Outline each uninfected red blood cell.
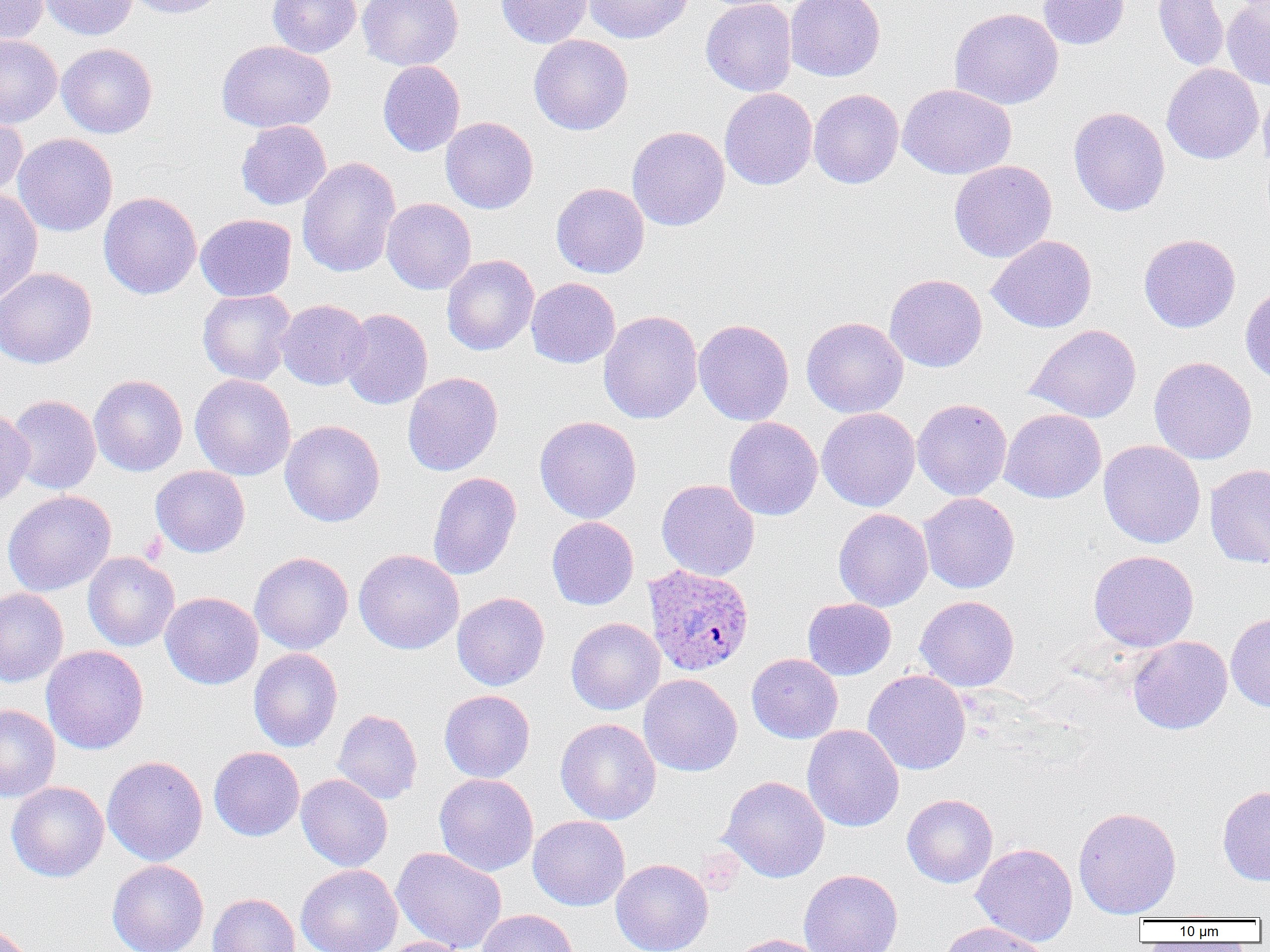
Approximate bounding boxes as named x1/y1/x2/y2 corners in pixels.
Uninfected red blood cells: (x1=0, y1=0, x2=48, y2=44), (x1=39, y1=0, x2=137, y2=40), (x1=124, y1=0, x2=228, y2=19), (x1=268, y1=0, x2=361, y2=58), (x1=358, y1=0, x2=463, y2=71), (x1=495, y1=0, x2=594, y2=48), (x1=584, y1=0, x2=692, y2=44), (x1=701, y1=0, x2=797, y2=96), (x1=785, y1=0, x2=885, y2=82), (x1=1037, y1=0, x2=1130, y2=49), (x1=1153, y1=0, x2=1229, y2=71), (x1=1222, y1=0, x2=1270, y2=90), (x1=949, y1=7, x2=1063, y2=110), (x1=529, y1=34, x2=633, y2=135), (x1=0, y1=35, x2=62, y2=128), (x1=216, y1=40, x2=336, y2=133), (x1=57, y1=43, x2=158, y2=138), (x1=378, y1=61, x2=465, y2=156), (x1=1162, y1=63, x2=1263, y2=164), (x1=897, y1=83, x2=1016, y2=179), (x1=1258, y1=83, x2=1270, y2=175), (x1=719, y1=88, x2=818, y2=190), (x1=809, y1=89, x2=904, y2=188), (x1=1068, y1=106, x2=1170, y2=217), (x1=0, y1=110, x2=27, y2=202), (x1=440, y1=116, x2=538, y2=213), (x1=236, y1=120, x2=331, y2=210), (x1=626, y1=125, x2=730, y2=231), (x1=13, y1=133, x2=117, y2=236), (x1=297, y1=157, x2=400, y2=277), (x1=949, y1=160, x2=1056, y2=262), (x1=551, y1=182, x2=650, y2=278), (x1=0, y1=189, x2=43, y2=304), (x1=99, y1=192, x2=201, y2=299), (x1=382, y1=198, x2=476, y2=294), (x1=196, y1=213, x2=296, y2=302), (x1=1138, y1=233, x2=1240, y2=333), (x1=987, y1=235, x2=1097, y2=333), (x1=442, y1=255, x2=538, y2=355), (x1=0, y1=267, x2=98, y2=368), (x1=884, y1=273, x2=987, y2=372), (x1=526, y1=277, x2=620, y2=368), (x1=1240, y1=284, x2=1270, y2=386), (x1=197, y1=289, x2=296, y2=385), (x1=276, y1=299, x2=370, y2=390), (x1=339, y1=308, x2=433, y2=410), (x1=598, y1=310, x2=703, y2=424), (x1=801, y1=317, x2=908, y2=418), (x1=693, y1=319, x2=794, y2=425), (x1=1025, y1=324, x2=1142, y2=423), (x1=1149, y1=356, x2=1257, y2=465), (x1=402, y1=372, x2=503, y2=476), (x1=89, y1=374, x2=188, y2=476), (x1=190, y1=374, x2=296, y2=481), (x1=6, y1=395, x2=101, y2=494), (x1=912, y1=398, x2=1012, y2=501), (x1=0, y1=406, x2=34, y2=509), (x1=817, y1=407, x2=920, y2=511), (x1=999, y1=409, x2=1106, y2=503), (x1=535, y1=415, x2=642, y2=523), (x1=723, y1=417, x2=823, y2=520), (x1=280, y1=420, x2=385, y2=527), (x1=1098, y1=440, x2=1205, y2=548), (x1=1205, y1=464, x2=1270, y2=568), (x1=150, y1=466, x2=250, y2=557), (x1=428, y1=472, x2=521, y2=580), (x1=656, y1=479, x2=760, y2=581), (x1=3, y1=490, x2=116, y2=596), (x1=918, y1=492, x2=1020, y2=594), (x1=833, y1=508, x2=933, y2=612), (x1=547, y1=517, x2=639, y2=610), (x1=354, y1=549, x2=464, y2=654), (x1=1088, y1=550, x2=1199, y2=652), (x1=249, y1=551, x2=354, y2=654), (x1=83, y1=552, x2=180, y2=651), (x1=0, y1=588, x2=68, y2=687), (x1=160, y1=592, x2=263, y2=689), (x1=452, y1=592, x2=550, y2=690), (x1=915, y1=595, x2=1019, y2=692), (x1=803, y1=598, x2=896, y2=680), (x1=1226, y1=612, x2=1270, y2=712), (x1=566, y1=617, x2=665, y2=715), (x1=1128, y1=636, x2=1232, y2=734), (x1=41, y1=645, x2=148, y2=754), (x1=248, y1=648, x2=343, y2=752), (x1=746, y1=653, x2=843, y2=743), (x1=863, y1=670, x2=971, y2=775), (x1=639, y1=673, x2=742, y2=776), (x1=439, y1=690, x2=535, y2=783), (x1=0, y1=705, x2=61, y2=802), (x1=332, y1=709, x2=423, y2=805), (x1=555, y1=718, x2=661, y2=824), (x1=802, y1=724, x2=904, y2=832), (x1=209, y1=746, x2=304, y2=841), (x1=102, y1=755, x2=208, y2=866), (x1=434, y1=773, x2=538, y2=876), (x1=296, y1=774, x2=393, y2=871), (x1=719, y1=776, x2=830, y2=882), (x1=7, y1=781, x2=109, y2=882), (x1=1217, y1=785, x2=1270, y2=886), (x1=902, y1=794, x2=998, y2=887), (x1=1073, y1=806, x2=1181, y2=918), (x1=528, y1=815, x2=630, y2=911), (x1=971, y1=843, x2=1078, y2=947), (x1=391, y1=846, x2=507, y2=952), (x1=611, y1=858, x2=713, y2=952), (x1=107, y1=859, x2=209, y2=952), (x1=296, y1=864, x2=402, y2=952), (x1=799, y1=869, x2=904, y2=952), (x1=208, y1=893, x2=300, y2=952), (x1=477, y1=909, x2=578, y2=952), (x1=939, y1=921, x2=1049, y2=952), (x1=0, y1=923, x2=34, y2=952), (x1=728, y1=934, x2=827, y2=952), (x1=376, y1=937, x2=470, y2=952).

Summary:
  - Plasmodium ovale-infected red blood cell locations: (x1=642, y1=564, x2=754, y2=677)
  - Slide-level diagnosis: Plasmodium ovale
  - Modality: light microscopy
  - Field of view: single
  - Preparation: thin blood film
  - Magnification: 1000x
  - Image size: 1270×952 pixels